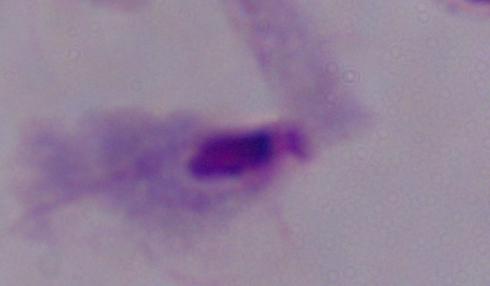
Photomicrograph. A trichomonad is shown. 1000x magnification.